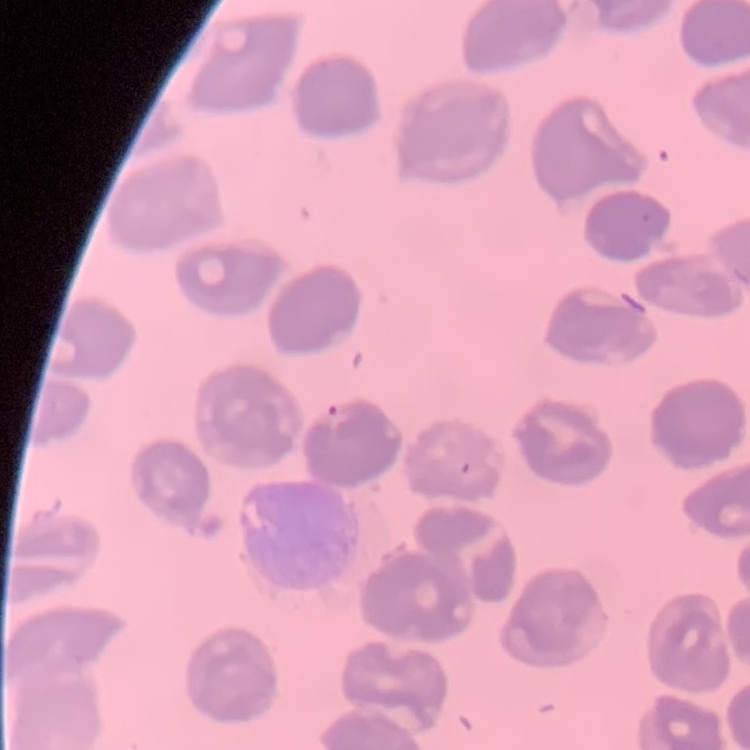
Summary:
  - Erythrocyte morphology: no rouleaux formation
  - Image type: square crop of a larger photomicrograph
  - Stain: Field's or Giemsa
  - Preparation: thin blood film